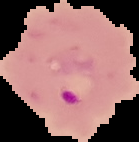
Summary:
  - Image size: 139×142 pixels
  - Preparation: thin blood smear
  - Image type: segmented cell region with the area outside set to black
  - Malaria status: parasitized